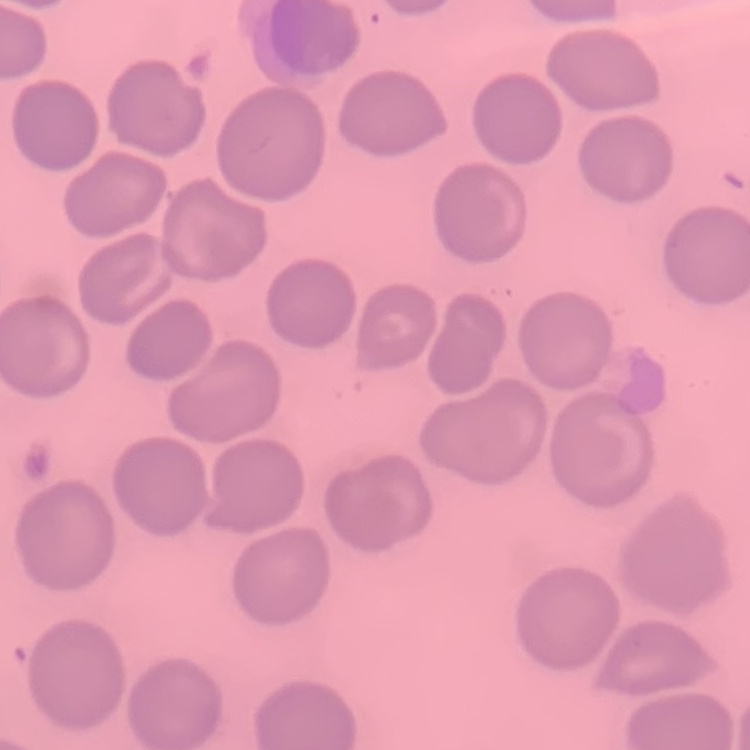

{
  "red_blood_cell_morphology": "no rouleaux formation",
  "image_type": "square crop of a larger photomicrograph",
  "stain": "Field's or Giemsa",
  "preparation": "thin peripheral smear"
}